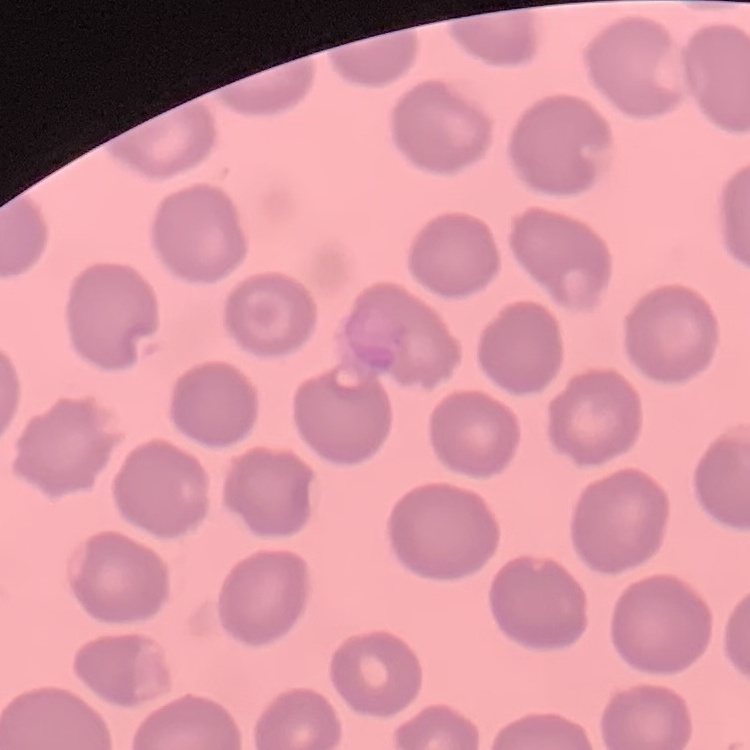

erythrocyte_morphology: no rouleaux formation
preparation: thin peripheral smear
image_type: square crop of a larger photomicrograph
stain: Field's or Giemsa